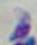
{
  "identification": "Toxoplasma gondii",
  "modality": "micrograph",
  "magnification": "1000x"
}